Identify the parasite.
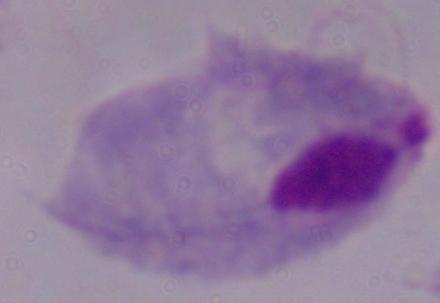

A trichomonad.

{
  "magnification": "1000x",
  "modality": "photomicrograph"
}